Give the extent of all uninfected red blood cells.
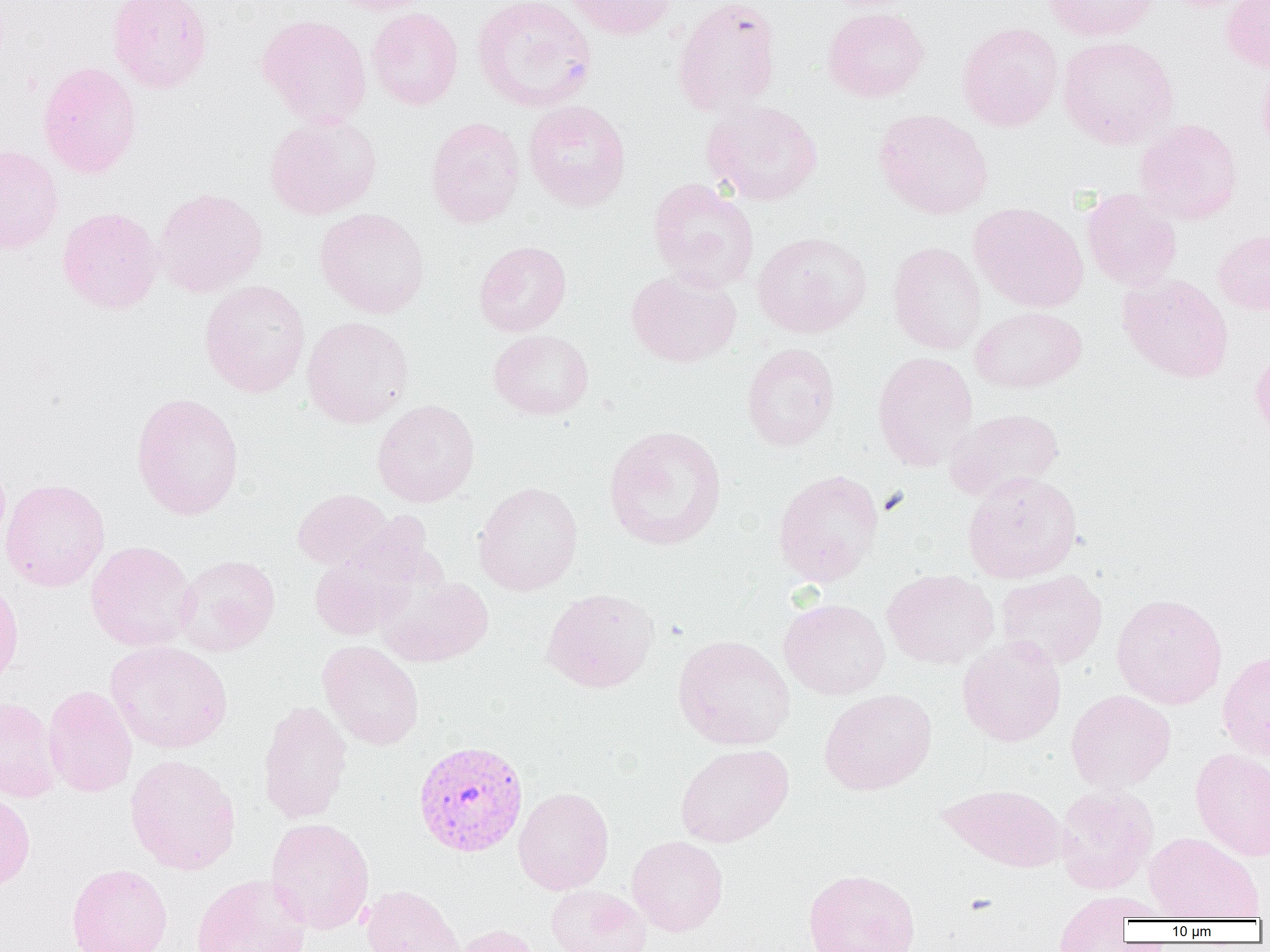
Approximate bounding boxes as (x1, y1, x2, y2) in pixels.
Uninfected red blood cells: (107, 0, 213, 93), (327, 0, 435, 15), (563, 0, 678, 40), (671, 0, 781, 116), (1043, 0, 1157, 41), (1221, 0, 1270, 73), (472, 1, 597, 112), (367, 7, 463, 109), (822, 7, 929, 102), (257, 14, 372, 128), (956, 21, 1063, 131), (1057, 36, 1178, 149), (1256, 59, 1270, 163), (37, 61, 142, 178), (701, 99, 823, 205), (524, 100, 630, 211), (873, 109, 994, 219), (264, 114, 381, 219), (425, 117, 525, 228), (1134, 118, 1242, 225), (0, 145, 63, 255), (647, 178, 759, 292), (153, 187, 267, 297), (1081, 188, 1182, 289), (969, 202, 1088, 313), (58, 207, 163, 314), (315, 207, 429, 318), (752, 230, 871, 338), (1212, 230, 1270, 316), (474, 240, 572, 337), (887, 242, 986, 355), (626, 269, 741, 367), (1118, 274, 1233, 383), (199, 280, 311, 397), (970, 306, 1087, 393), (302, 316, 414, 428), (488, 329, 594, 420), (1250, 342, 1270, 446), (741, 343, 840, 451), (872, 351, 978, 472), (131, 392, 245, 520), (372, 399, 480, 507), (944, 408, 1064, 500), (603, 424, 727, 551), (0, 457, 11, 551), (772, 469, 884, 587), (962, 471, 1082, 583), (1, 478, 110, 592), (473, 481, 584, 596), (292, 488, 393, 570), (308, 531, 434, 641), (85, 540, 197, 651), (174, 554, 280, 656), (882, 569, 999, 669), (996, 569, 1107, 669), (378, 574, 494, 667), (0, 579, 24, 688), (540, 587, 660, 693), (1111, 593, 1228, 709), (779, 598, 890, 700), (673, 635, 795, 750), (957, 635, 1066, 747), (105, 640, 233, 753), (317, 640, 425, 750), (1218, 649, 1270, 762), (42, 685, 137, 798), (819, 688, 937, 795), (1066, 689, 1176, 792), (0, 696, 63, 802), (257, 701, 353, 824), (675, 743, 794, 848), (1190, 748, 1270, 861), (125, 754, 241, 875), (938, 783, 1067, 873), (1054, 785, 1159, 894), (513, 787, 614, 895), (0, 790, 36, 893), (265, 817, 374, 934), (1144, 832, 1263, 920), (627, 835, 728, 936), (66, 863, 173, 952), (803, 868, 921, 952), (191, 873, 312, 952), (359, 885, 466, 952), (546, 885, 651, 952), (1053, 892, 1151, 951), (454, 924, 543, 952).

Summary:
  - Plasmodium vivax-infected red blood cell locations: (412, 740, 529, 857)
  - Slide-level diagnosis: Plasmodium vivax
  - Magnification: 1000x
  - Image size: 1270×952 pixels
  - Preparation: thin blood film
  - Modality: optical microscopy
  - Field of view: single